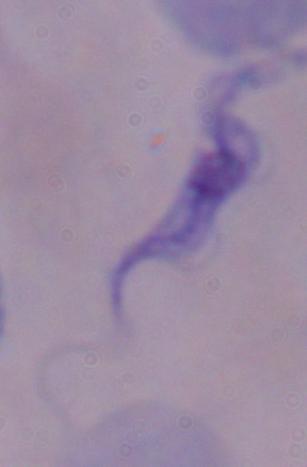
Summary:
  - Identification: trypanosome
  - Modality: photomicrograph
  - Magnification: 1000x